State which parasite is depicted.
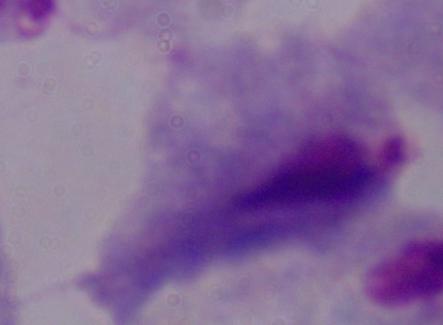

This is a trichomonad.

magnification = 1000x
modality = micrograph